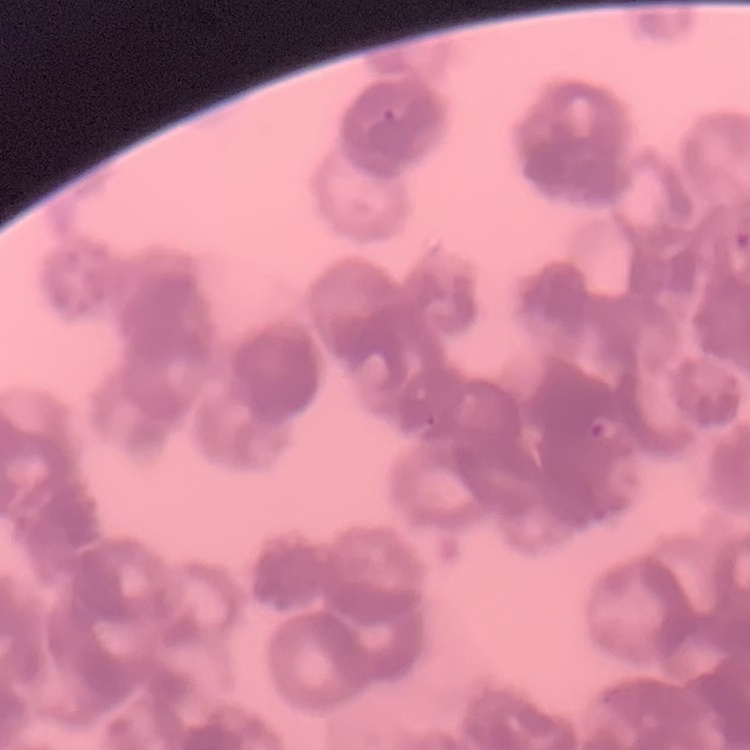

Summary:
  - Red blood cell morphology: rouleaux formation
  - Stain: Field's or Giemsa
  - Image type: square crop of a larger photomicrograph
  - Preparation: thin blood smear